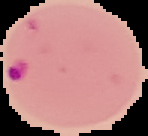

Summary:
  - Image size: 148×136 pixels
  - Preparation: thin blood smear
  - Result: malaria parasites detected
  - Image type: segmented cell region with the area outside set to black